Name the cell type shown.
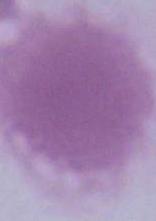
This is an erythrocyte.

Summary:
  - Modality: photomicrograph
  - Magnification: 1000x